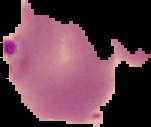
Summary:
  - Image type: cell region segmented out of the field of view; surrounding area masked to black
  - Image size: 151×127 pixels
  - Preparation: thin blood film
  - Malaria status: parasitized